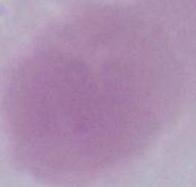

1000x magnification. Photomicrograph. An erythrocyte is seen.